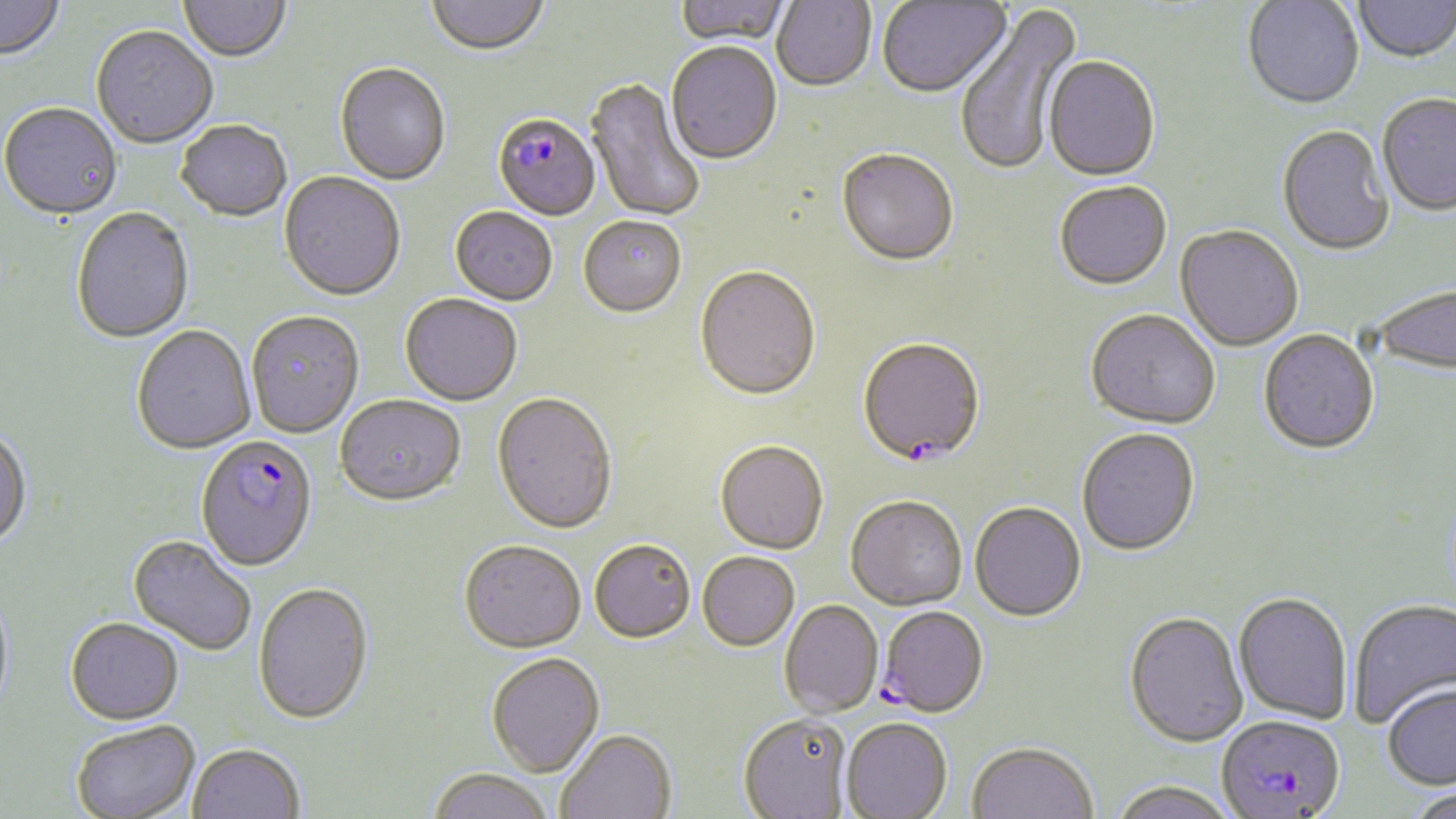

Approximate bounding boxes as (x1,y1)-(x2,y2) corner pairs in pixels. Plasmodium falciparum-infected red blood cell locations: (492,116)-(601,222), (857,341)-(986,470), (195,436)-(318,573), (878,607)-(989,719), (1217,716)-(1346,818). Uninfected red blood cell locations: (0,0)-(64,64), (426,0)-(550,58), (673,0)-(792,48), (1353,0)-(1455,66), (178,1)-(290,65), (772,1)-(876,93), (1243,1)-(1364,113), (877,2)-(1012,101), (954,4)-(1084,177), (91,27)-(218,151), (665,44)-(783,166), (1043,58)-(1161,183), (335,64)-(451,187), (585,78)-(706,223), (1378,96)-(1456,218), (1,105)-(123,222), (176,122)-(292,224), (1277,126)-(1393,258), (836,152)-(958,269), (279,173)-(405,303), (1054,183)-(1172,293), (71,209)-(194,345), (450,209)-(558,308), (579,218)-(686,319), (1174,227)-(1303,353), (695,269)-(821,404), (1375,286)-(1456,377), (400,295)-(522,408), (246,312)-(364,440), (1085,312)-(1220,431), (132,327)-(256,456), (1258,331)-(1380,458), (491,394)-(618,536), (335,398)-(466,510), (0,427)-(32,552), (1077,429)-(1200,558), (714,443)-(828,556), (845,498)-(967,613), (970,503)-(1086,623), (127,536)-(256,657), (589,542)-(696,645), (459,543)-(586,656), (697,554)-(799,653), (0,584)-(15,725), (254,585)-(374,727), (1233,594)-(1352,725), (1348,599)-(1456,730), (779,600)-(883,719), (1123,613)-(1248,749), (65,620)-(184,727), (486,654)-(605,779), (1382,683)-(1456,791), (738,715)-(853,819), (841,718)-(952,818), (71,723)-(200,819), (556,731)-(677,819), (967,742)-(1098,819), (188,746)-(304,819), (427,771)-(554,819), (1106,781)-(1238,819), (1405,785)-(1456,819). Slide-level diagnosis: Plasmodium falciparum. Image is 1456×819 pixels. Captured at 1000x magnification. Optical microscopy. May-Grünwald-Giemsa-stained preparation. One field of a larger specimen. Thin blood film.